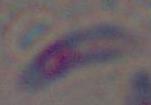

Summary:
  - Identification: Toxoplasma gondii
  - Magnification: 1000x
  - Modality: photomicrograph